Locate every Plasmodium falciparum-infected red blood cell.
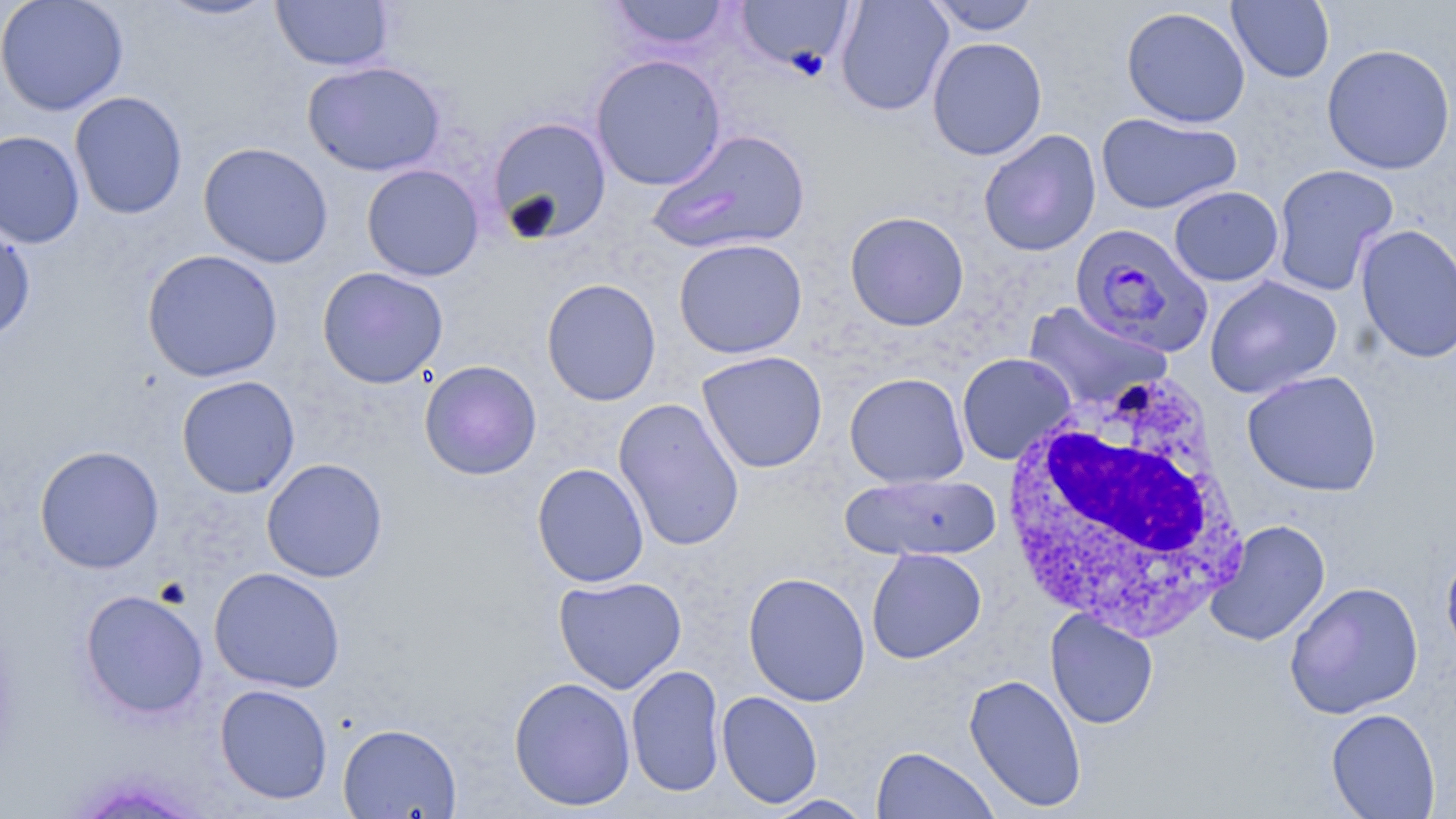

Approximate bounding boxes as (x1, y1, x2, y2) in pixels.
Plasmodium falciparum-infected red blood cells: (1069, 223, 1213, 357).

{
  "slide_level_diagnosis": "Plasmodium falciparum",
  "magnification": "1000x",
  "uninfected_red_blood_cell_locations": "approximate bounding boxes as (x1, y1, x2, y2) in pixels: (0, 0, 129, 116), (153, 0, 282, 21), (270, 0, 395, 71), (607, 0, 733, 50), (734, 0, 855, 75), (835, 0, 954, 116), (926, 0, 1041, 35), (1227, 0, 1334, 84), (1121, 6, 1251, 128), (927, 37, 1047, 161), (1321, 43, 1455, 175), (590, 53, 726, 190), (302, 59, 446, 177), (69, 91, 188, 219), (1096, 112, 1243, 214), (488, 116, 612, 244), (650, 128, 811, 255), (978, 129, 1101, 257), (0, 130, 85, 249), (199, 142, 333, 268), (361, 163, 484, 281), (1271, 163, 1399, 296), (1169, 186, 1284, 286), (844, 211, 969, 331), (0, 223, 36, 344), (1355, 223, 1456, 364), (673, 238, 808, 359), (141, 249, 283, 382), (316, 267, 448, 388), (1205, 275, 1343, 399), (541, 278, 661, 405), (1022, 301, 1172, 413), (696, 350, 828, 473), (957, 353, 1076, 464), (419, 360, 542, 480), (1242, 370, 1382, 497), (844, 372, 969, 488), (176, 375, 301, 498), (613, 397, 745, 551), (34, 444, 164, 574), (261, 458, 388, 582), (532, 463, 649, 587), (840, 472, 1001, 562), (1206, 520, 1330, 647), (1441, 543, 1456, 664), (866, 547, 986, 664), (209, 566, 345, 693), (743, 571, 871, 707), (553, 575, 687, 694), (1284, 581, 1424, 719), (79, 589, 209, 719), (1045, 609, 1159, 729), (626, 664, 726, 797), (964, 673, 1088, 812), (508, 676, 636, 811), (214, 683, 333, 804), (716, 691, 823, 808), (1325, 708, 1441, 819), (338, 723, 462, 819), (871, 745, 999, 818), (764, 794, 874, 818)",
  "white_blood_cell_locations": "approximate bounding boxes as (x1, y1, x2, y2) in pixels: (998, 370, 1248, 642)",
  "modality": "optical microscopy",
  "image_size": "1456×819 pixels",
  "preparation": "thin blood smear",
  "stain": "May-Grünwald-Giemsa",
  "field_of_view": "single"
}